Locate every malaria parasite.
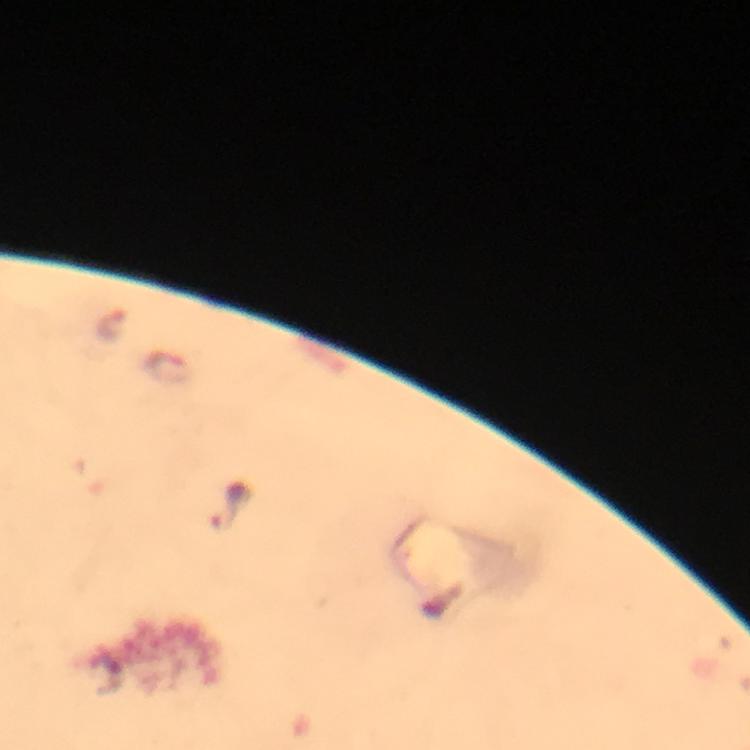
Approximate centers as [x, y] in pixels.
Malaria parasites: [111, 325], [170, 369], [229, 505].

Summary:
  - Stain: Giemsa
  - Cropped from: a single field of view
  - Immersion oil: applied
  - Magnification: 100x
  - Preparation: thick blood smear
  - Image size: 750×750 pixels
  - Capture: smartphone photograph through a microscope
  - Context: from a diagnostic examination for malaria